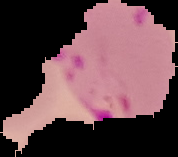

From a thin blood smear. Image is 178×157 pixels. Malaria status: parasitized. The area outside the segmented cell region is set to black.